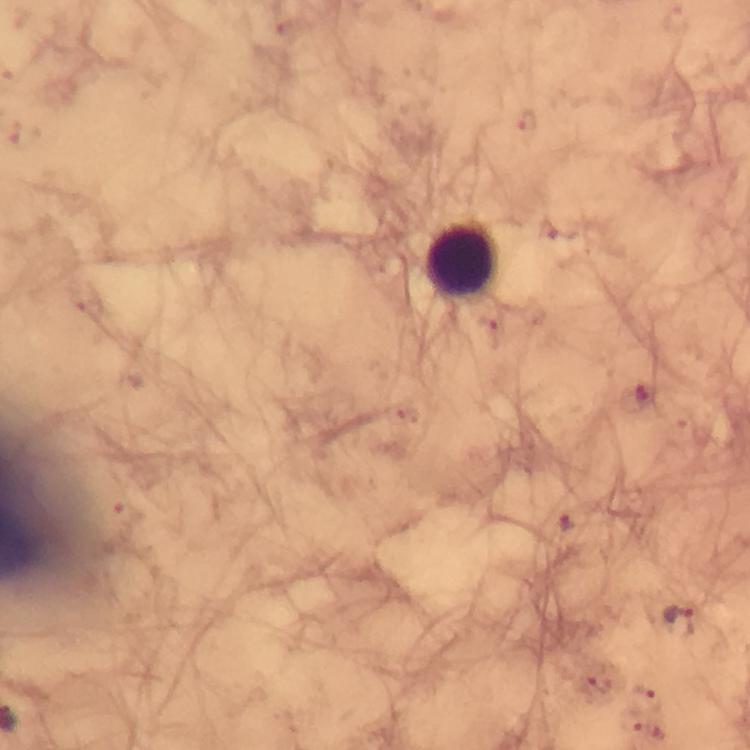

Approximate centers as (x, y) in pixels.
Summary:
  - Malaria parasite locations: (677, 620)
  - Leukocyte locations: (465, 263)
  - Capture: smartphone photograph through a microscope
  - Stain: Giemsa
  - Cropped from: one field of view
  - Preparation: thick blood smear
  - Image size: 750×750 pixels
  - Magnification: 100x
  - Immersion oil: applied
  - Context: from a malaria diagnostic workup